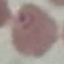

Result: malaria parasites identified. Thin smear of blood. Cell patch, automatically extracted from a larger field of view and resized to 64 × 64 pixels. Photographed with a smartphone camera at the microscope eyepiece. Giemsa-stained preparation.